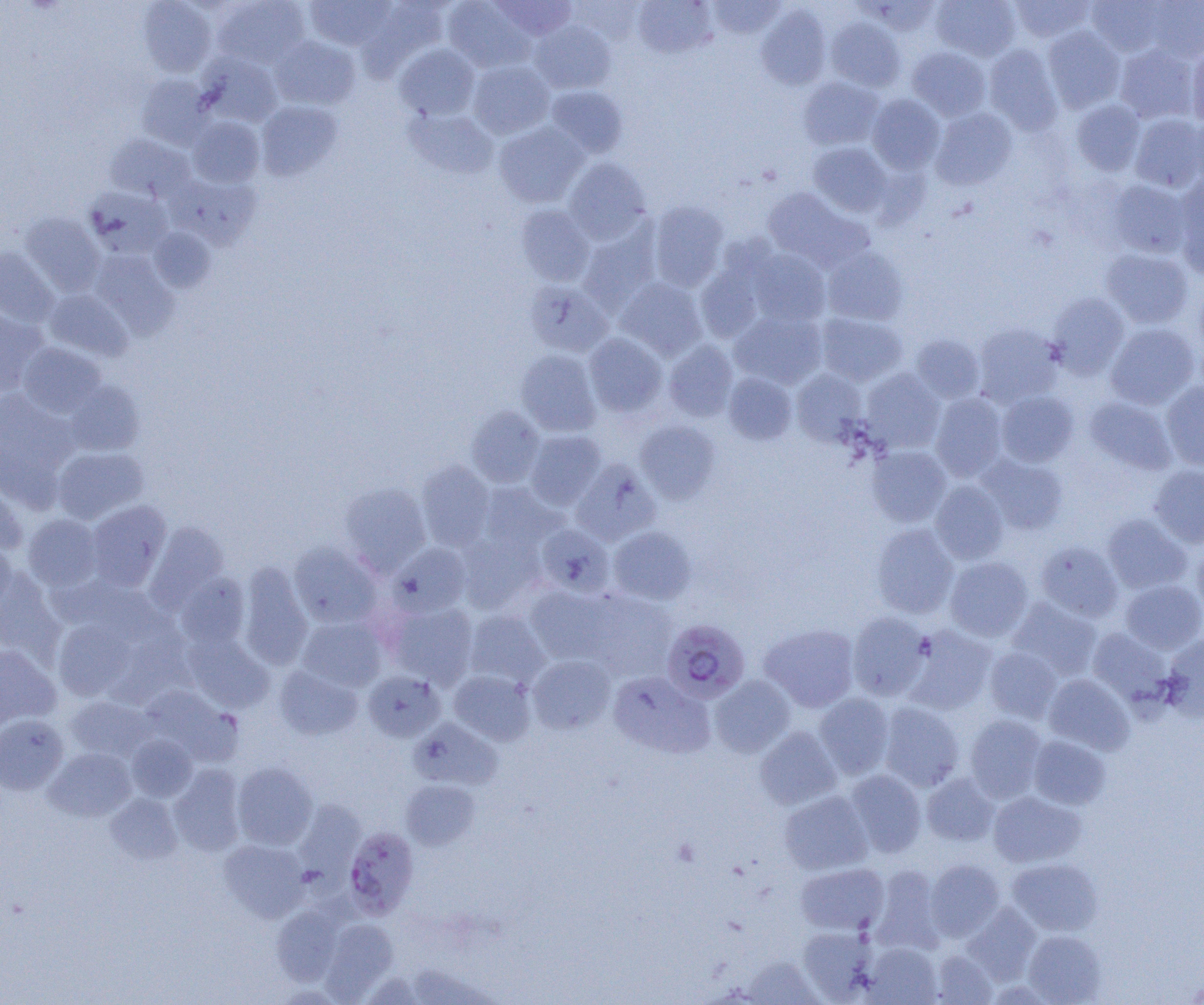
slide_level_diagnosis: Plasmodium falciparum
modality: optical microscopy
magnification: 1000x
preparation: thin blood film
plasmodium_falciparum_infected_red_blood_cell_locations: 'approximate bounding boxes as (x1,y1)-(x2,y2) corner pairs in pixels: (661,619)-(750,703), (344,827)-(418,918)'
uninfected_red_blood_cell_locations: 'approximate bounding boxes as (x1,y1)-(x2,y2) corner pairs in pixels: (138,0)-(216,77), (213,0)-(310,68), (491,0)-(576,40), (708,0)-(785,38), (869,0)-(942,36), (931,0)-(1021,62), (1010,0)-(1095,43), (1087,0)-(1167,57), (305,1)-(394,50), (357,1)-(450,80), (443,1)-(535,73), (633,1)-(715,58), (1144,1)-(1204,61), (756,5)-(831,89), (826,18)-(904,91), (530,21)-(616,93), (1042,26)-(1125,113), (270,36)-(360,109), (394,44)-(480,121), (984,44)-(1063,135), (1115,45)-(1197,123), (1186,45)-(1204,127), (908,47)-(991,121), (198,53)-(282,127), (468,60)-(555,139), (136,74)-(213,149), (799,77)-(884,151), (546,85)-(628,158), (867,95)-(945,174), (1071,99)-(1145,175), (256,101)-(342,179), (404,108)-(499,179), (930,108)-(1017,189), (1190,112)-(1204,186), (1130,114)-(1204,192), (188,117)-(264,187), (493,122)-(589,207), (105,134)-(194,202), (808,142)-(892,217), (564,158)-(651,244), (167,173)-(261,250), (1175,175)-(1204,275), (1109,180)-(1192,258), (86,188)-(172,258), (762,188)-(872,271), (647,202)-(729,291), (515,205)-(595,286), (20,213)-(104,296), (578,224)-(661,312), (149,227)-(215,292), (0,247)-(59,326), (822,247)-(908,326), (748,248)-(831,327), (1101,248)-(1193,328), (92,251)-(178,339), (696,259)-(766,342), (616,278)-(707,360), (526,280)-(613,357), (1193,283)-(1204,369), (45,289)-(132,361), (1047,292)-(1130,378), (0,310)-(48,395), (731,311)-(827,389), (816,312)-(907,386), (1106,323)-(1199,409), (974,324)-(1064,407), (584,333)-(667,417), (910,334)-(985,403), (663,340)-(738,422), (18,343)-(106,418), (516,350)-(600,436), (791,369)-(868,447), (860,369)-(945,453), (724,372)-(797,444), (65,380)-(145,456), (1161,381)-(1204,471), (0,389)-(78,499), (995,391)-(1079,467), (930,393)-(1009,481), (1084,396)-(1176,475), (466,407)-(545,488), (635,420)-(720,504), (525,430)-(606,510), (867,445)-(952,527), (53,447)-(149,524), (977,454)-(1068,534), (571,459)-(660,545), (416,462)-(495,551), (1149,465)-(1204,548), (0,481)-(27,555), (930,481)-(1009,564), (340,482)-(431,574), (478,482)-(565,554), (86,500)-(171,591), (1102,514)-(1191,594), (23,515)-(103,591), (146,522)-(229,612), (871,523)-(959,619), (535,524)-(616,598), (609,526)-(697,604), (456,532)-(544,613), (0,539)-(17,615), (1036,540)-(1123,622), (289,542)-(382,629), (388,543)-(471,617), (1192,543)-(1204,619), (945,556)-(1033,642), (238,563)-(313,670), (0,570)-(65,664), (176,574)-(249,649), (1120,579)-(1204,654), (526,585)-(613,664), (578,589)-(679,679), (1008,599)-(1102,681), (385,601)-(478,688), (464,610)-(549,689), (847,612)-(931,701), (54,617)-(135,702), (298,617)-(386,692), (760,623)-(860,712), (903,625)-(997,714), (1087,627)-(1172,704), (1161,632)-(1204,721), (184,633)-(274,712), (0,644)-(61,729), (985,647)-(1062,724), (527,655)-(615,734), (274,665)-(362,740), (449,669)-(536,745), (363,671)-(444,742), (609,671)-(713,758), (1044,674)-(1134,754), (710,676)-(795,757), (142,686)-(241,766), (815,693)-(894,779), (66,696)-(154,761), (878,702)-(964,791), (0,714)-(68,795), (965,714)-(1047,801), (412,718)-(503,789), (755,726)-(841,810), (127,735)-(197,801), (1028,735)-(1111,809), (44,747)-(136,822), (232,762)-(318,850), (169,765)-(246,856), (844,769)-(926,857), (922,773)-(998,846), (401,780)-(480,850), (779,790)-(873,875), (988,791)-(1086,868), (106,794)-(182,864), (298,802)-(366,900), (219,840)-(309,922), (1007,858)-(1102,936), (925,859)-(1005,941), (796,862)-(889,935), (870,865)-(946,954), (962,904)-(1041,984), (272,906)-(343,986), (320,918)-(398,1001), (798,925)-(877,1002), (1023,929)-(1106,1004), (862,942)-(942,1004), (930,949)-(998,1005), (740,955)-(822,1004), (1183,976)-(1204,1004)'
image_size: 1204×1005 pixels
field_of_view: one of a larger specimen